Locate and identify every blood parasite.
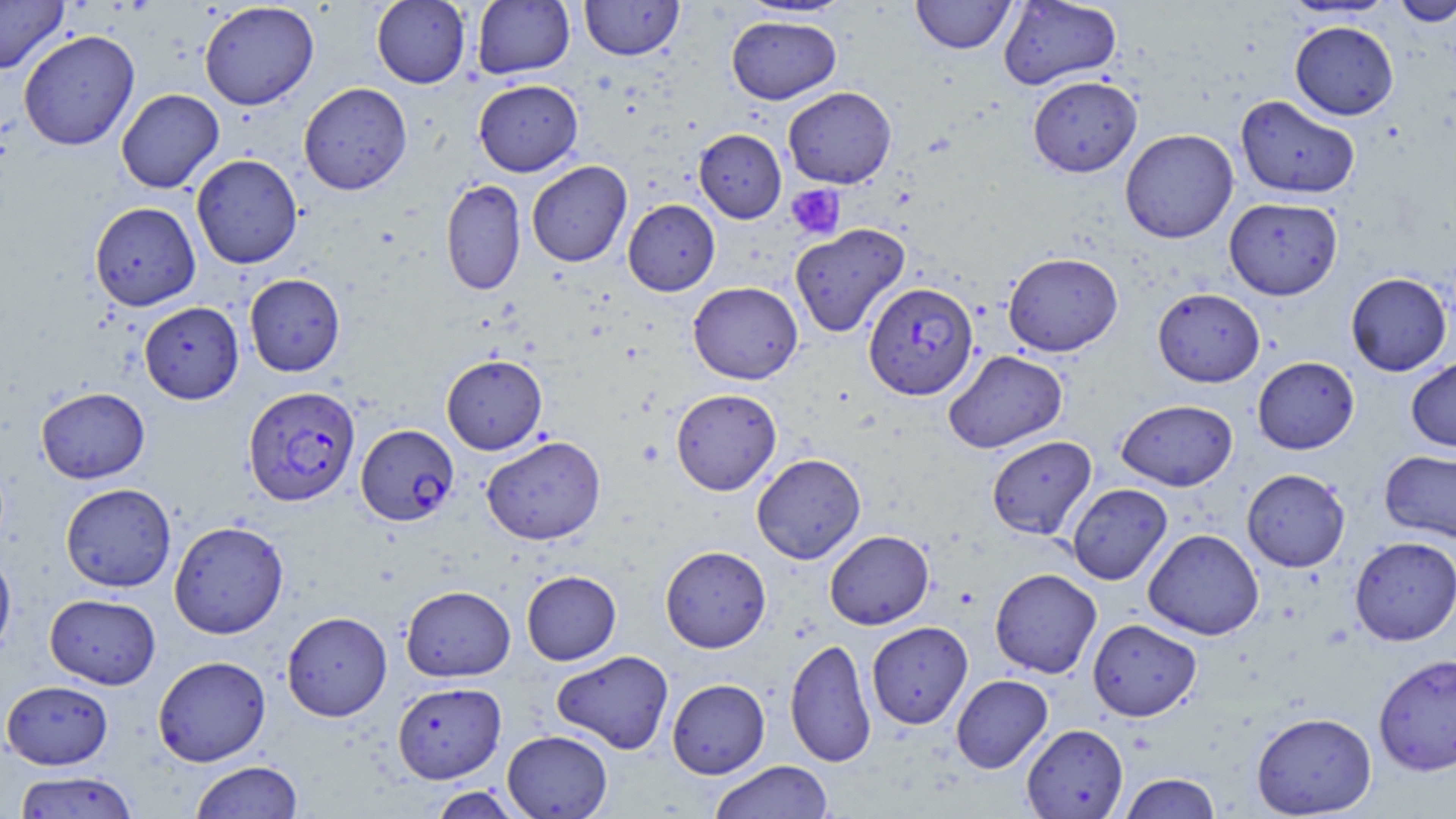

Approximate bounding boxes as (x1,y1)-(x2,y2) corner pairs in pixels.
Plasmodium falciparum-infected red blood cells: (864,281)-(978,400), (243,386)-(360,507), (356,424)-(459,526).
No Plasmodium ovale, Plasmodium malariae, Plasmodium vivax, Babesia divergens, or Trypanosoma brucei observed.

Summary:
  - Platelet locations: (786,184)-(845,240)
  - Uninfected red blood cell locations: (0,0)-(69,74), (371,0)-(471,88), (472,0)-(575,79), (579,0)-(684,61), (911,0)-(1016,54), (998,0)-(1122,90), (1392,0)-(1456,27), (199,1)-(319,110), (734,1)-(856,20), (726,16)-(841,104), (1289,20)-(1399,120), (18,30)-(140,151), (1028,75)-(1141,177), (473,79)-(583,176), (298,82)-(412,195), (782,86)-(897,188), (116,89)-(224,193), (1235,95)-(1360,199), (694,129)-(786,223), (1120,129)-(1238,243), (191,154)-(303,269), (526,160)-(632,267), (440,178)-(526,296), (1224,197)-(1343,300), (623,199)-(720,296), (89,202)-(201,311), (789,223)-(910,338), (1002,252)-(1123,356), (1345,272)-(1452,376), (244,273)-(345,376), (688,282)-(803,384), (1152,287)-(1265,387), (139,301)-(244,404), (944,350)-(1068,453), (441,354)-(547,454), (1407,356)-(1456,451), (1252,357)-(1359,454), (36,387)-(150,483), (671,388)-(781,495), (1116,399)-(1238,490), (482,435)-(606,545), (986,435)-(1097,540), (1380,450)-(1456,543), (752,453)-(866,564), (1242,469)-(1350,572), (60,482)-(176,592), (1066,483)-(1172,585), (169,520)-(289,639), (1143,529)-(1264,640), (824,530)-(934,629), (1349,536)-(1456,646), (660,545)-(771,652), (0,549)-(16,661), (990,568)-(1102,678), (521,570)-(621,665), (400,585)-(515,682), (45,593)-(160,689), (282,611)-(392,721), (1087,618)-(1201,721), (867,621)-(973,728), (784,637)-(876,767), (551,650)-(674,754), (1373,654)-(1456,776), (153,655)-(271,766), (951,674)-(1052,773), (667,678)-(770,778), (1,680)-(114,769), (392,681)-(506,783), (1252,712)-(1377,817), (1021,724)-(1128,818), (503,730)-(612,819), (190,760)-(303,818), (708,760)-(833,818), (13,771)-(139,818), (1119,773)-(1222,818), (427,786)-(526,818)
  - Slide-level diagnosis: Plasmodium falciparum
  - Magnification: 1000x
  - Stain: May-Grünwald-Giemsa
  - Modality: optical microscopy
  - Image size: 1456×819 pixels
  - Preparation: thin blood smear
  - Field of view: one of a larger specimen